Assess the morphology of the red blood cells.
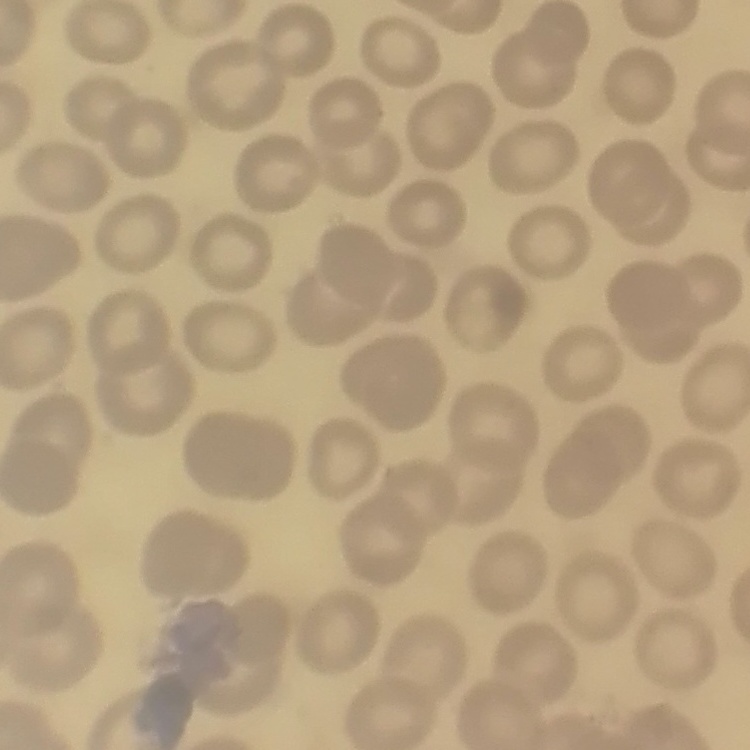

They show no rouleaux formation.

Thin blood film. One tile cut from a larger photomicrograph. Field's or Giemsa stain.